Assess the morphology of the erythrocytes.
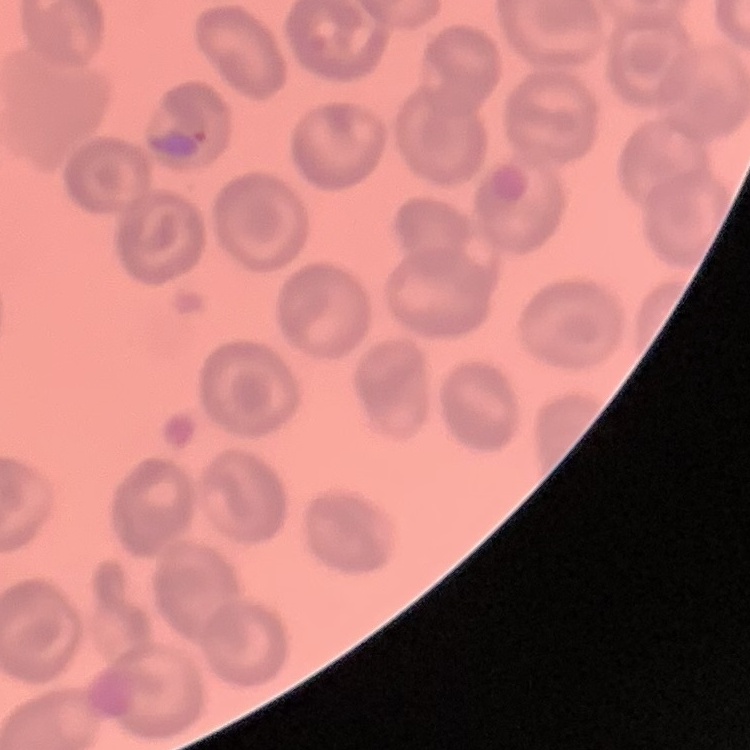

No rouleaux formation.

stain = Field's or Giemsa
image type = square crop of a larger photomicrograph
preparation = thin blood film